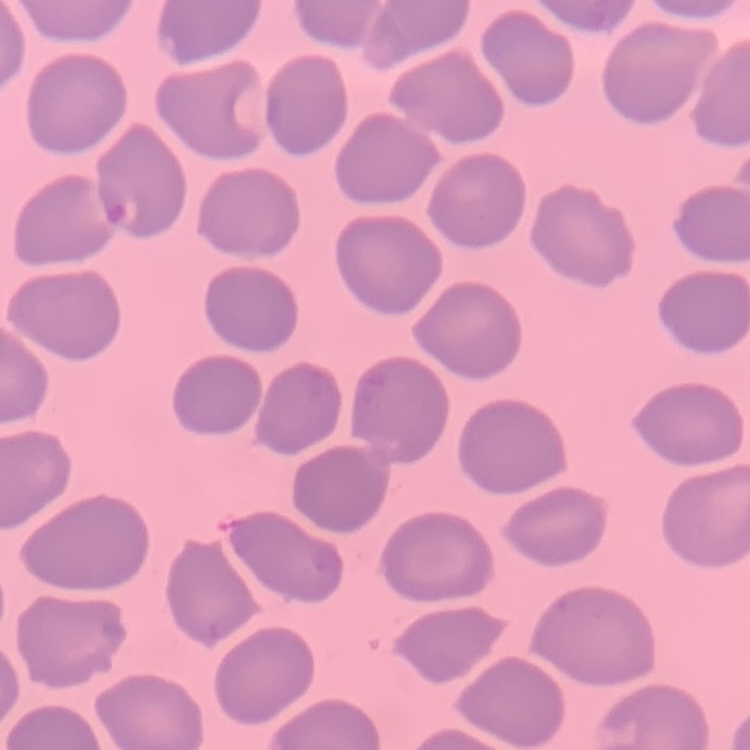
red blood cell morphology = no rouleaux formation
preparation = thin blood smear
image type = square crop of a larger photomicrograph
stain = Field's or Giemsa